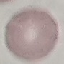 Malaria status: uninfected. Cell patch, automatically extracted from a larger field of view and resized to 64 × 64 pixels. Giemsa-stained preparation. Thin blood film. Photographed with a smartphone camera at the microscope eyepiece.